Report the malaria status of this cell.
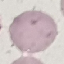

It is uninfected.

Thin blood smear. Cell patch, automatically extracted from a larger field of view and resized to 64 × 64 pixels. Giemsa stain. Acquired by smartphone through the microscope eyepiece.